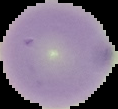

The area outside the segmented cell region is set to black. Image is 118×109 pixels. From a thin blood smear. Result: no Plasmodium parasites detected.